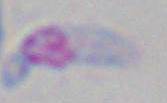

Summary:
  - Magnification: 1000x
  - Identification: Toxoplasma gondii
  - Modality: micrograph